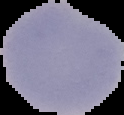 From a thin blood smear. Result: malaria parasites detected. The area outside the segmented cell region is set to black. Image is 124×115 pixels.